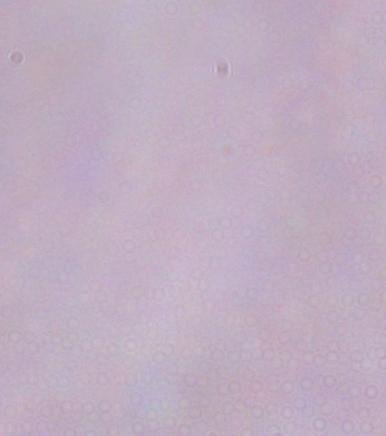

1000x magnification. Micrograph. A trypanosome is seen.